Describe the morphology of the erythrocytes.
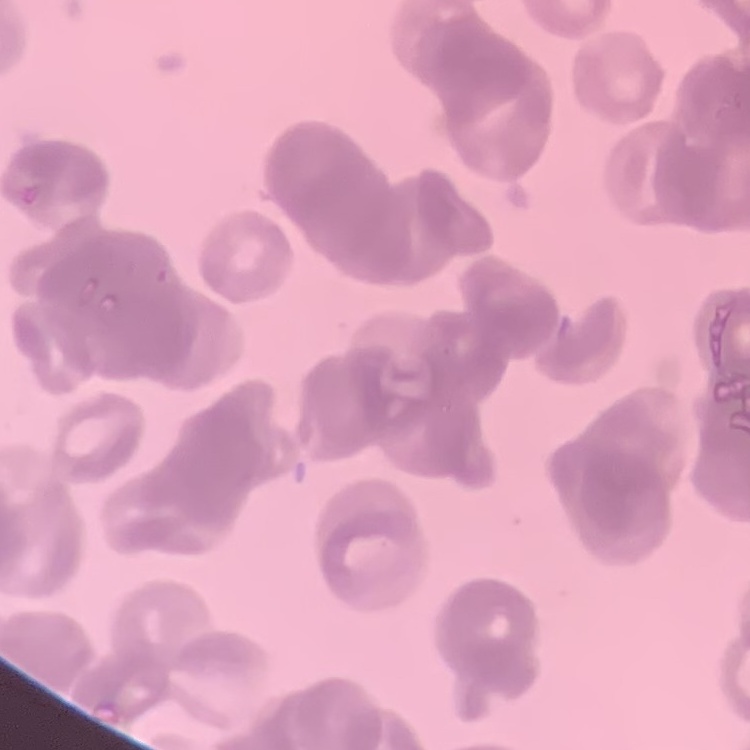

They show rouleaux formation.

Thin peripheral smear. Stained with either Field's or Giemsa. Square crop of a larger photomicrograph.